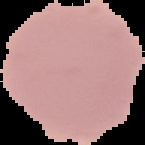
From a thin blood smear. Image is 145×145 pixels. Cell region segmented out of the field of view; the surrounding area is masked to black. Result: no malaria parasites detected.